Name the cell type shown.
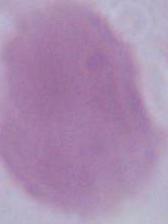
This is an erythrocyte.

Summary:
  - Magnification: 1000x
  - Modality: micrograph